Give the position of every Plasmodium parasite.
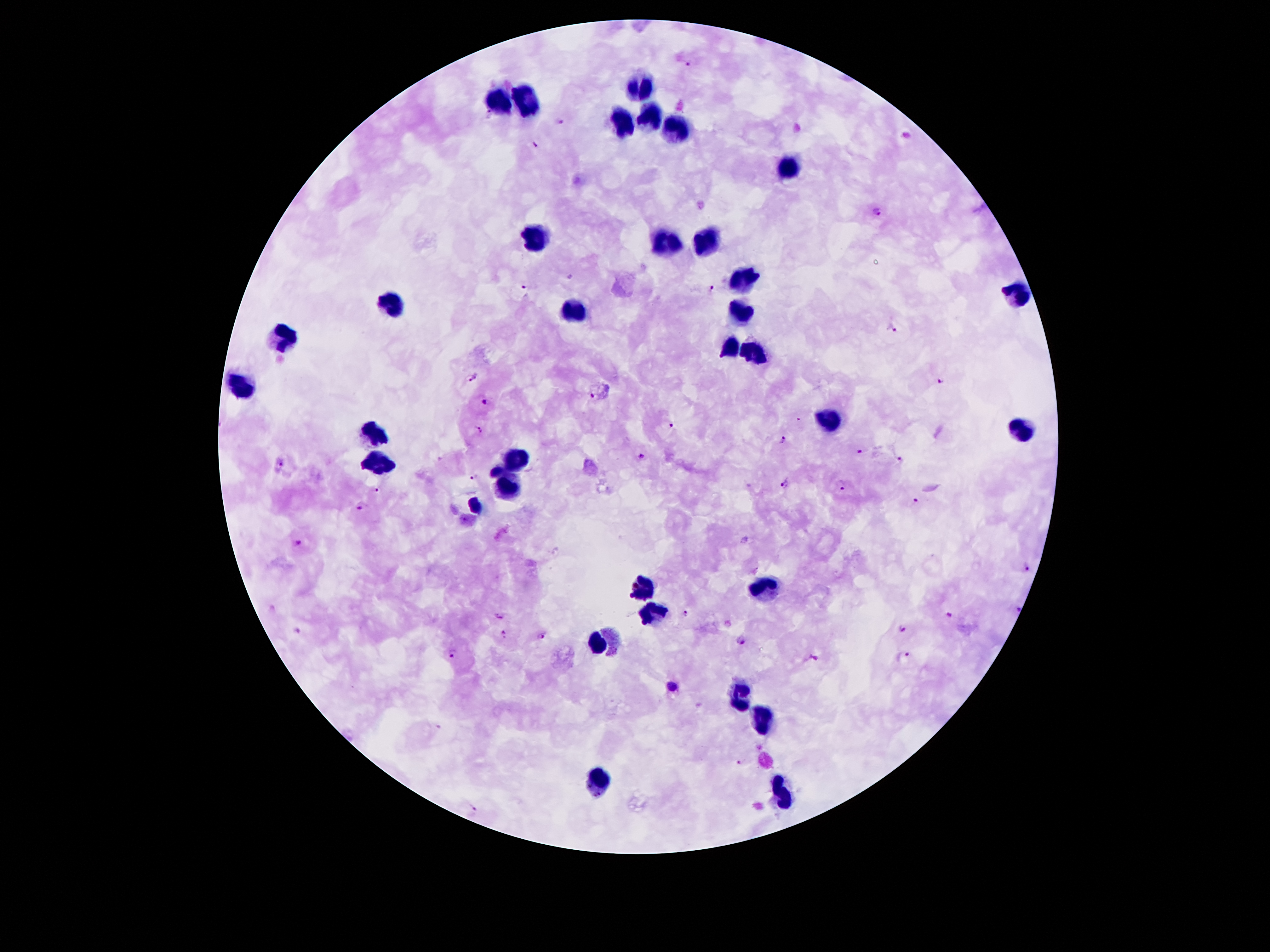

Approximate centers as (x, y) in pixels.
Plasmodium parasites: (686, 63), (488, 115), (558, 122), (535, 144), (878, 213), (525, 288), (713, 289), (892, 330), (472, 375), (938, 381), (593, 395), (484, 402), (670, 425), (481, 429), (783, 438), (860, 450), (642, 456), (902, 458), (279, 463), (475, 476), (783, 483), (843, 486), (378, 489), (915, 502), (361, 508), (296, 542), (1026, 567), (686, 610), (499, 614), (949, 614), (902, 628), (299, 632), (504, 633), (541, 637), (741, 640), (452, 652), (817, 658), (903, 659), (671, 687), (738, 763), (474, 809).

leukocyte locations = (640, 87), (496, 97), (520, 101), (650, 117), (620, 119), (676, 129), (790, 167), (536, 236), (664, 239), (710, 239), (742, 280), (1016, 294), (394, 301), (572, 305), (738, 309), (280, 339), (730, 344), (752, 350), (240, 386), (828, 421), (376, 433), (1020, 433), (516, 463), (380, 465), (508, 487), (476, 508), (644, 584), (772, 591), (652, 615), (596, 638), (736, 695), (762, 723), (600, 782), (786, 797)
stain = Giemsa
field of view = single
preparation = thick peripheral-blood smear
image size = 1270×952 pixels
magnification = 100x
patient malaria status = infected with Plasmodium falciparum
capture = smartphone camera through the microscope eyepiece